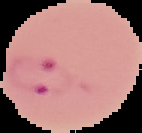

Segmented cell region on a black background. Malaria status: parasitized. Image is 142×133 pixels. From a thin blood smear.